Give the extent of all Babesia divergens-infected red blood cells.
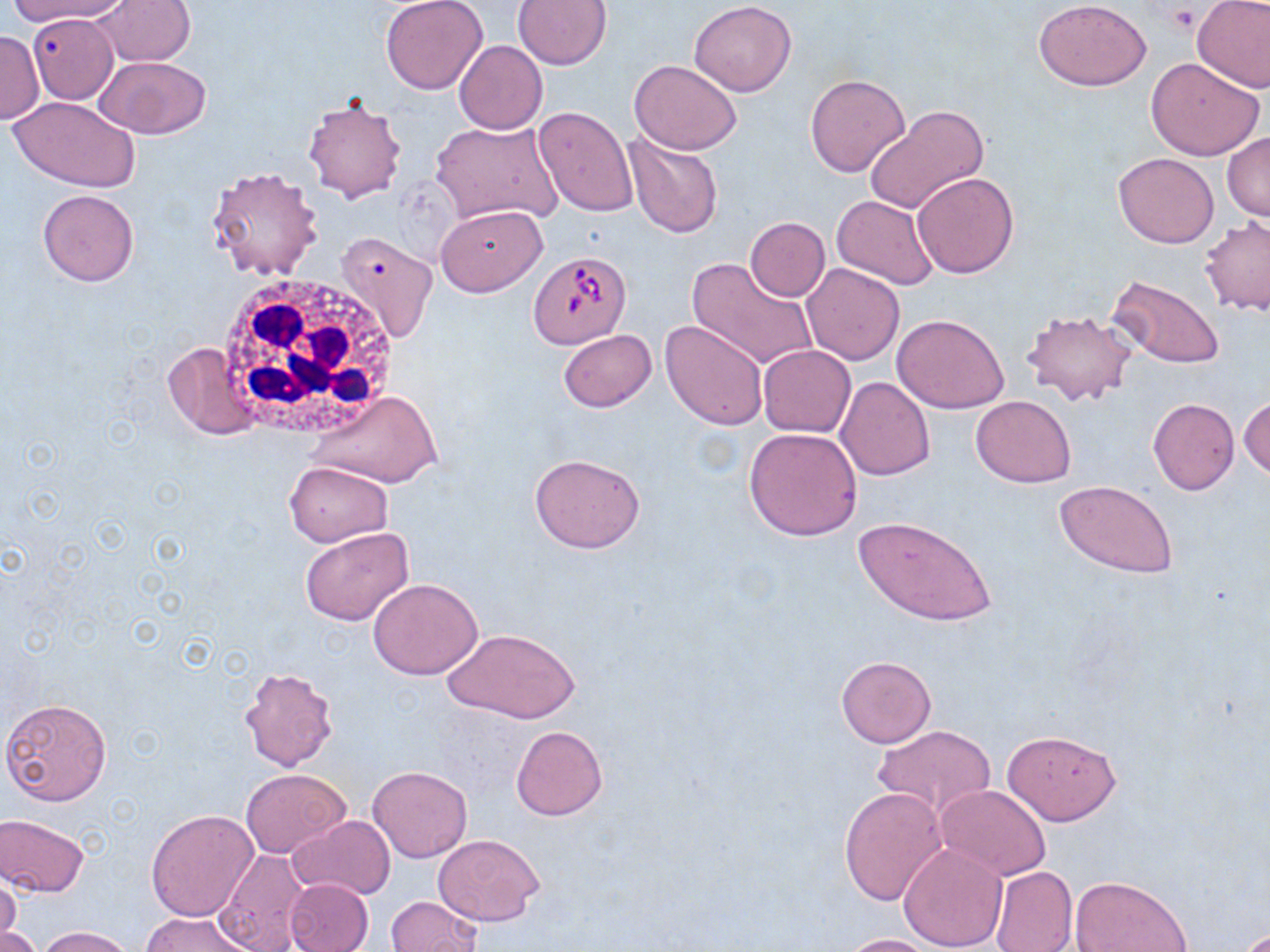
Approximate bounding boxes as (x1, y1, x2, y2) in pixels.
Babesia divergens-infected red blood cells: (526, 251, 632, 350).

slide_level_diagnosis: Babesia divergens
field_of_view: single
modality: light microscopy
image_size: 1270×952 pixels
magnification: 1000x
stain: May-Grünwald-Giemsa
uninfected_red_blood_cell_locations: 'approximate bounding boxes as (x1, y1, x2, y2) in pixels: (6, 0, 125, 26), (92, 0, 198, 67), (380, 0, 488, 95), (513, 0, 612, 69), (1034, 0, 1151, 91), (1192, 0, 1270, 92), (689, 1, 797, 96), (28, 14, 120, 103), (0, 31, 43, 124), (453, 40, 548, 134), (1145, 56, 1265, 161), (95, 57, 211, 139), (629, 59, 742, 154), (805, 73, 911, 176), (302, 95, 407, 203), (9, 96, 140, 192), (533, 106, 638, 217), (865, 106, 989, 216), (432, 120, 564, 226), (1222, 132, 1270, 223), (625, 134, 723, 238), (1113, 152, 1219, 248), (205, 167, 324, 281), (911, 171, 1020, 279), (37, 189, 140, 286), (830, 195, 939, 290), (435, 205, 547, 296), (1200, 215, 1270, 315), (744, 217, 830, 301), (335, 231, 438, 343), (687, 256, 819, 372), (801, 262, 904, 365), (1106, 275, 1225, 369), (1022, 308, 1136, 409), (891, 313, 1010, 414), (661, 318, 769, 430), (557, 330, 657, 412), (163, 342, 260, 439), (757, 344, 856, 438), (836, 376, 935, 480), (308, 390, 442, 489), (1239, 395, 1269, 482), (970, 396, 1077, 486), (1148, 398, 1240, 494), (744, 426, 862, 541), (530, 454, 645, 553), (284, 462, 392, 545), (1054, 480, 1179, 578), (855, 515, 996, 626), (298, 525, 416, 626), (368, 579, 481, 680), (445, 627, 580, 725), (835, 654, 937, 748), (238, 666, 339, 771), (1, 698, 112, 805), (872, 725, 995, 821), (511, 726, 607, 820), (1002, 729, 1121, 825), (366, 765, 473, 862), (241, 769, 350, 857), (935, 785, 1051, 880), (839, 787, 947, 908), (145, 808, 258, 922), (1, 814, 90, 897), (287, 816, 396, 901), (434, 834, 543, 926), (898, 843, 1008, 951), (215, 847, 308, 952), (990, 866, 1077, 952), (0, 873, 21, 949), (1070, 876, 1194, 952), (284, 878, 374, 952), (385, 896, 484, 952), (143, 911, 252, 952), (0, 922, 39, 952), (36, 925, 138, 952), (839, 933, 944, 952)'
white_blood_cell_locations: 'approximate bounding boxes as (x1, y1, x2, y2) in pixels: (213, 270, 399, 445)'
preparation: thin blood smear
platelet_locations: 'approximate bounding boxes as (x1, y1, x2, y2) in pixels: (1165, 4, 1204, 35)'